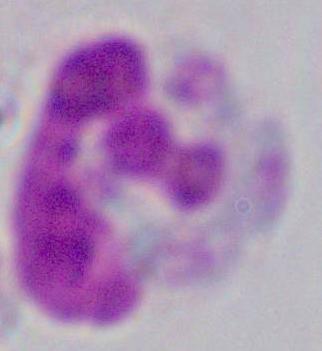 A leukocyte is seen. 1000x magnification. Photomicrograph.